Classify this cell by malaria status.
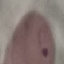

Parasitized.

Giemsa-stained preparation. Thin smear of blood. Acquired by smartphone through the microscope eyepiece. Automatically extracted cell patch, resized to 64 × 64 pixels.